Classify the preparation.
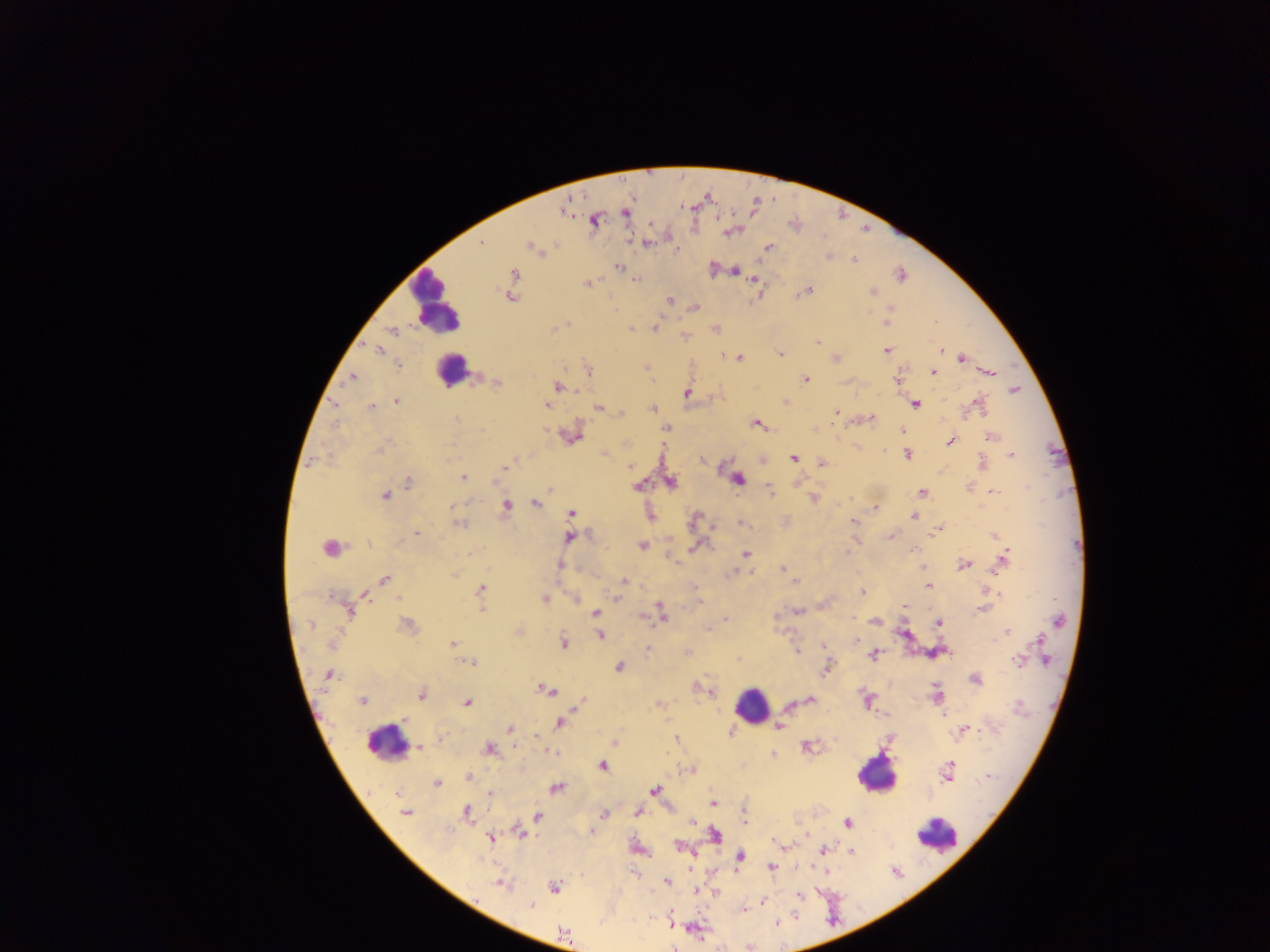

This is a thick smear.

field_of_view: single
capture: mobile-phone photograph through a microscope
country: Ghana
image_size: 1270×952 pixels
leukocyte_locations: 'approximate centers as x y in pixels: 435 304; 451 370; 751 706; 384 744; 875 774; 939 837'
plasmodium_parasite_locations: 'approximate centers as x y in pixels: 625 213; 595 220; 651 224; 647 243; 481 244; 532 247; 768 247; 677 250; 829 256; 853 259; 617 267; 735 271; 515 274; 901 275; 634 280; 756 280; 587 284; 809 291; 872 292; 510 297; 670 299; 695 308; 891 309; 885 322; 567 323; 654 328; 631 329; 392 331; 818 342; 941 349; 378 350; 887 351; 780 353; 723 355; 739 358; 836 359; 961 359; 398 366; 588 370; 932 372; 989 372; 352 377; 805 380; 898 381; 497 383; 558 387; 1014 390; 687 393; 396 401; 334 403; 978 403; 915 404; 547 406; 372 407; 598 407; 653 409; 835 412; 622 413; 870 418; 457 419; 756 424; 833 425; 665 428; 544 429; 903 430; 990 436; 572 437; 950 441; 379 449; 885 450; 604 454; 907 454; 1011 454; 793 458; 702 460; 310 462; 982 462; 822 463; 629 466; 504 467; 463 477; 737 479; 497 481; 408 482; 670 482; 638 486; 969 488; 550 490; 770 491; 993 491; 922 493; 385 495; 813 498; 535 503; 452 507; 505 507; 875 507; 571 514; 914 516; 650 517; 694 519; 853 522; 741 523; 459 524; 937 530; 416 533; 994 536; 568 537; 891 537; 999 539; 367 544; 642 545; 695 546; 328 548; 913 550; 746 553; 848 553; 1005 556; 964 564; 560 565; 1000 566; 783 570; 734 572; 455 574; 385 579; 624 580; 795 581; 929 586; 481 589; 862 592; 999 593; 332 598; 617 598; 544 599; 575 599; 905 606; 661 608; 983 609; 349 611; 798 611; 595 613; 662 613; 644 617; 726 619; 1058 621; 874 622; 939 623; 311 625; 407 625; 1007 632; 600 636; 856 640; 1038 641; 563 642; 332 643; 452 644; 823 646; 646 650; 796 651; 944 652; 879 658; 1017 660; 1045 660; 472 664; 619 667; 826 669; 329 674; 975 679; 542 689; 551 692; 710 692; 421 695; 936 695; 583 700; 362 701; 810 701; 467 703; 1018 707; 943 714; 403 719; 560 722; 779 726; 510 729; 963 730; 731 732; 537 737; 676 739; 615 743; 419 746; 806 746; 542 747; 489 749; 552 753; 772 756; 603 766; 948 769; 691 770; 947 776; 988 776; 468 778; 436 783; 556 787; 654 791; 396 794; 491 794; 713 803; 466 812; 637 812; 405 813; 604 815; 537 816; 745 822; 693 823; 847 823; 591 831; 520 832; 715 834; 490 839; 778 843; 677 845; 824 850; 851 852; 740 857; 771 867; 666 882; 501 884; 555 888; 697 891; 715 893; 799 896; 762 901; 531 905; 744 910; 777 924; 564 934; 674 948'